Report the malaria status of this cell.
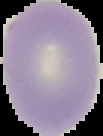
Uninfected.

preparation = thin blood film
image type = segmented cell region on a black background
image size = 103×136 pixels